Assess the morphology of the red blood cells.
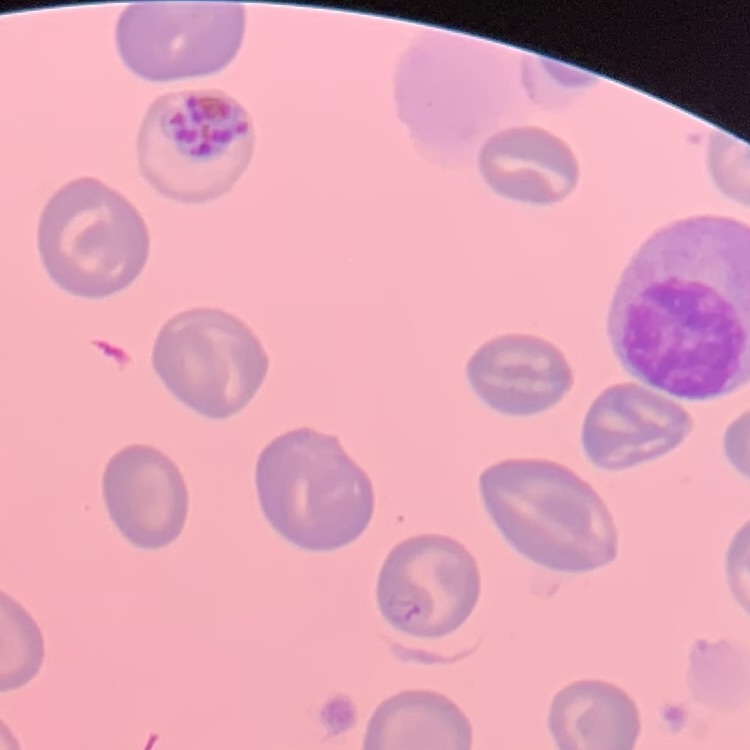

They show no rouleaux formation.

One tile cut from a larger photomicrograph. Field's or Giemsa stain. Thin blood smear.